Classify this cell by malaria status.
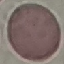
It is uninfected.

Photographed with a smartphone camera at the microscope eyepiece. Giemsa-stained preparation. Thin blood film. Automatically extracted cell patch, resized to 64 × 64 pixels.